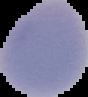
preparation: thin blood film
image_type: segmented cell region on a black background
image_size: 88×97 pixels
malaria_status: uninfected